Assess the morphology of the erythrocytes.
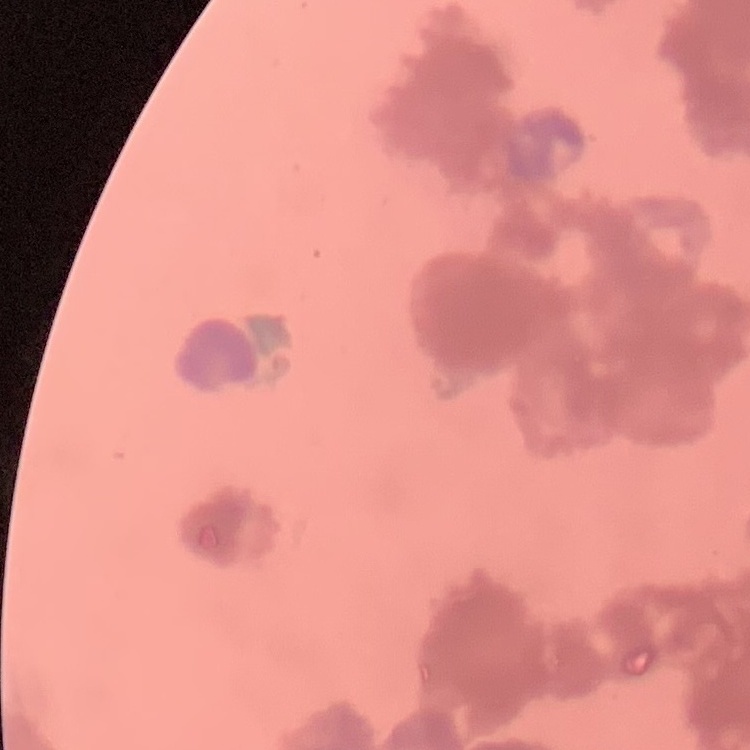
They show rouleaux formation.

preparation = thin blood smear
stain = Field's or Giemsa
image type = square crop of a larger photomicrograph